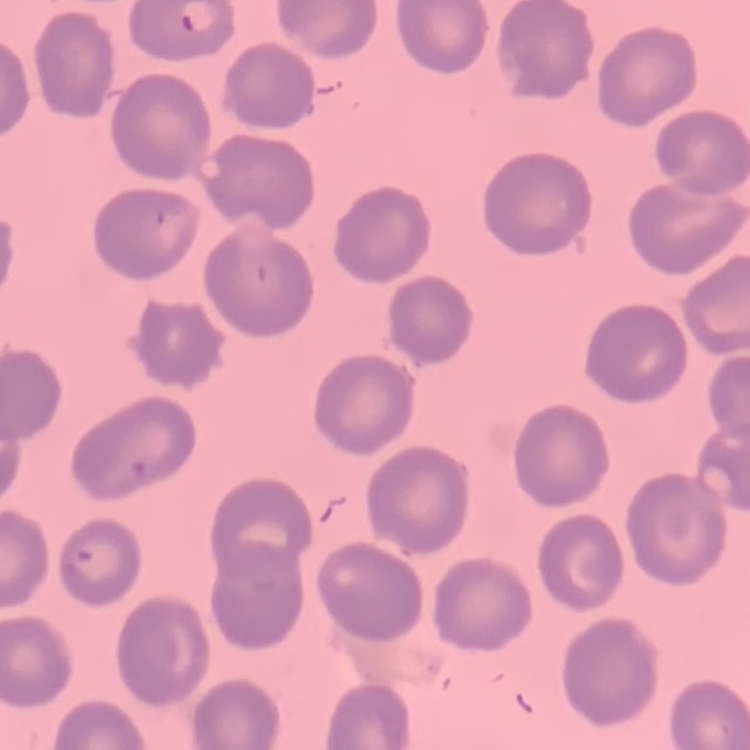 The erythrocytes exhibit no rouleaux formation. Field's or Giemsa stain. Thin blood film. One tile cut from a larger photomicrograph.